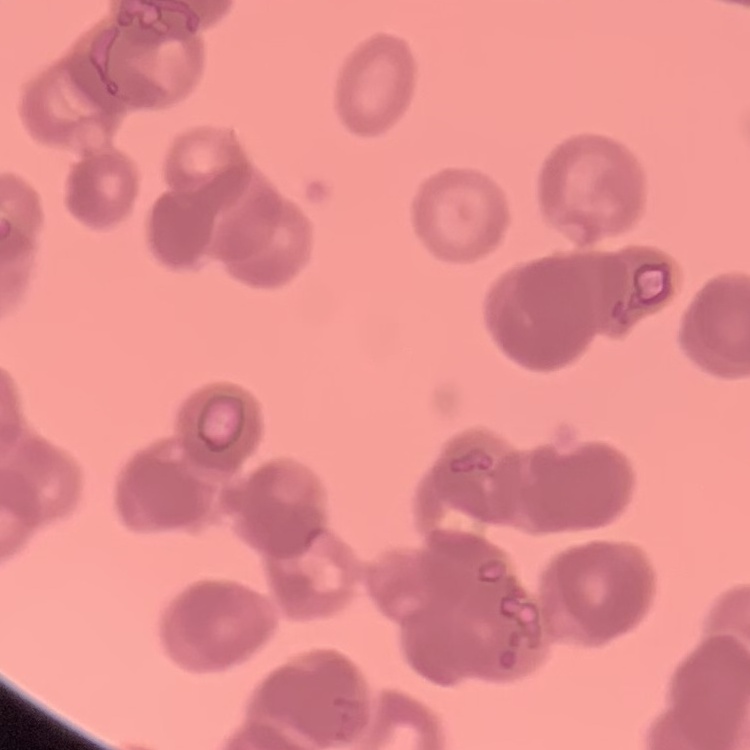

The erythrocytes exhibit rouleaux formation. Stained with either Field's or Giemsa. Thin blood film. One tile cut from a larger photomicrograph.